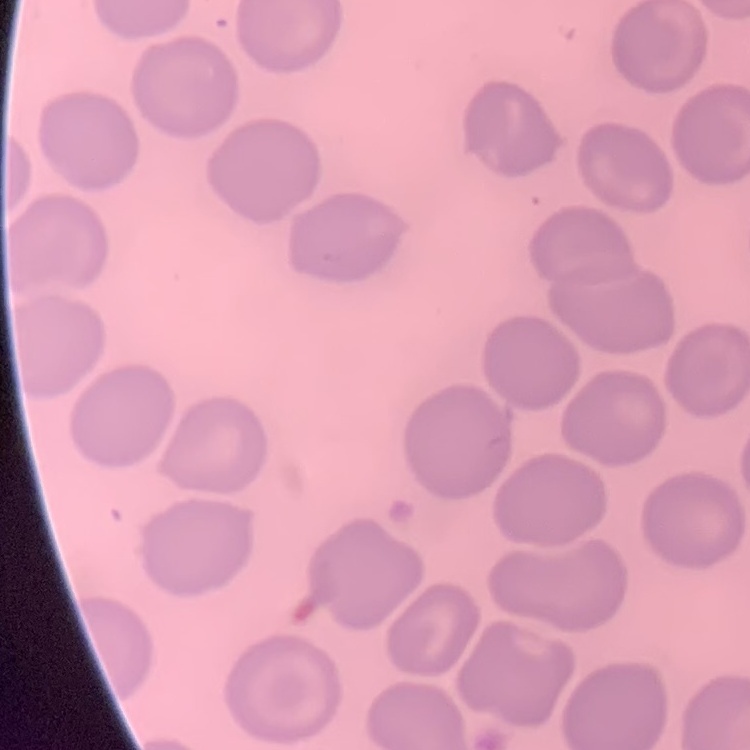 The red blood cells show no rouleaux formation. Square crop of a larger photomicrograph. Thin blood smear. Stained with either Field's or Giemsa.